Classify this cell by malaria status.
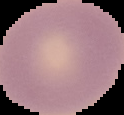

It is uninfected.

image type = segmented cell region on a black background
preparation = thin blood film
image size = 124×115 pixels